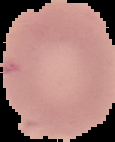 Result: negative for malaria parasites. From a thin blood smear. Image is 115×142 pixels. Segmented cell region on a black background.